Give the extent of all Plasmodium falciparum-infected red blood cells.
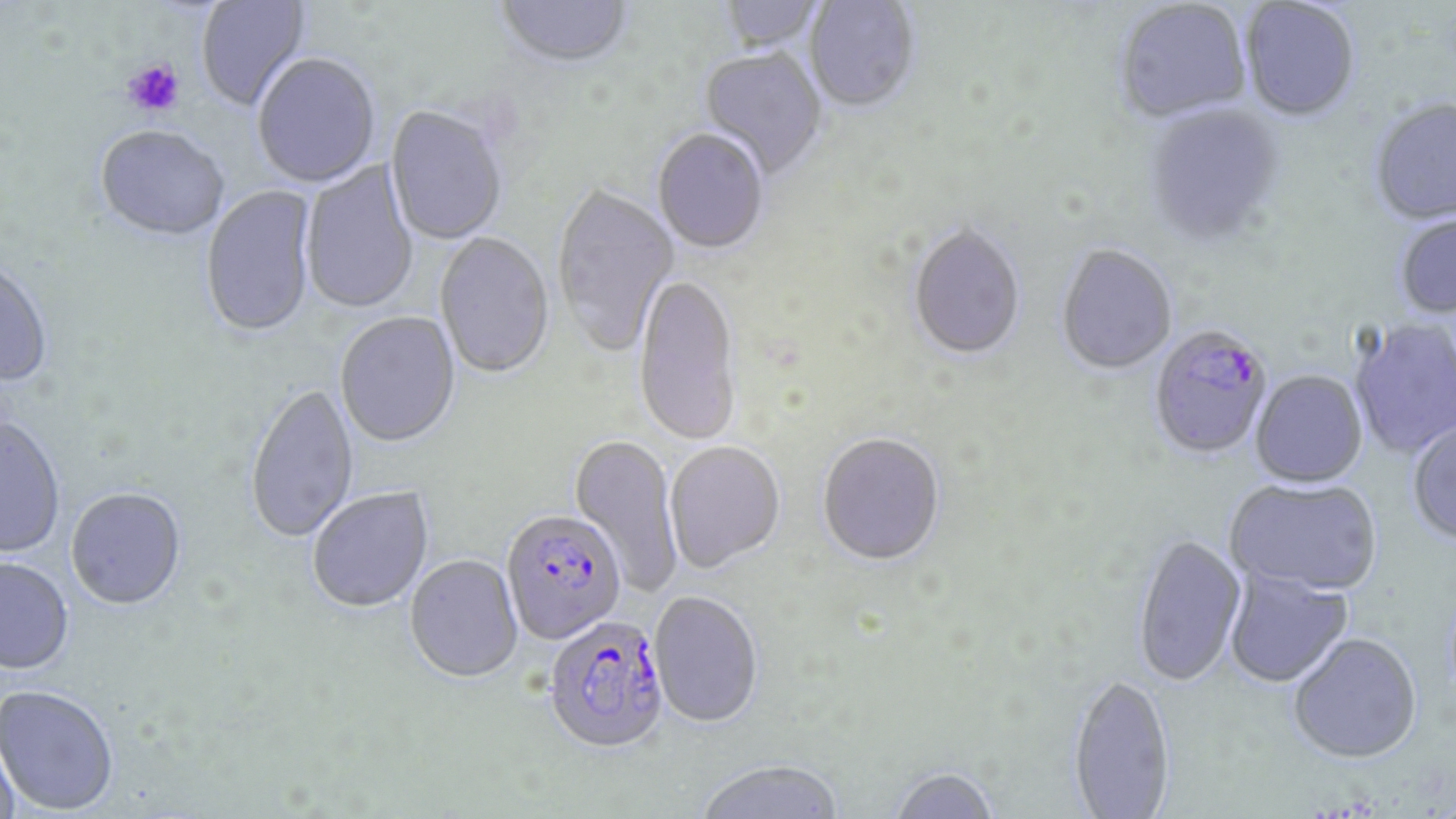
Approximate bounding boxes as named x1/y1/x2/y2 corners in pixels.
Plasmodium falciparum-infected red blood cells: (x1=1148, y1=328, x2=1274, y2=461), (x1=502, y1=513, x2=626, y2=647), (x1=543, y1=618, x2=670, y2=757).

Platelet locations: (x1=121, y1=58, x2=186, y2=118). Uninfected red blood cell locations: (x1=195, y1=1, x2=313, y2=114), (x1=495, y1=1, x2=635, y2=72), (x1=717, y1=1, x2=824, y2=55), (x1=804, y1=1, x2=920, y2=115), (x1=1115, y1=1, x2=1252, y2=125), (x1=1240, y1=1, x2=1360, y2=124), (x1=698, y1=49, x2=828, y2=181), (x1=252, y1=56, x2=381, y2=189), (x1=1370, y1=100, x2=1456, y2=228), (x1=1143, y1=105, x2=1284, y2=249), (x1=385, y1=107, x2=508, y2=246), (x1=94, y1=128, x2=229, y2=244), (x1=652, y1=130, x2=769, y2=255), (x1=300, y1=160, x2=419, y2=316), (x1=201, y1=185, x2=317, y2=341), (x1=551, y1=185, x2=679, y2=358), (x1=1395, y1=214, x2=1456, y2=320), (x1=908, y1=225, x2=1026, y2=364), (x1=434, y1=233, x2=555, y2=381), (x1=1056, y1=246, x2=1177, y2=377), (x1=0, y1=260, x2=54, y2=389), (x1=633, y1=276, x2=742, y2=448), (x1=335, y1=313, x2=461, y2=450), (x1=1348, y1=318, x2=1456, y2=461), (x1=1250, y1=371, x2=1368, y2=490), (x1=245, y1=384, x2=359, y2=545), (x1=0, y1=419, x2=66, y2=558), (x1=1407, y1=419, x2=1456, y2=547), (x1=569, y1=434, x2=682, y2=595), (x1=817, y1=434, x2=945, y2=569), (x1=664, y1=443, x2=786, y2=575), (x1=1225, y1=479, x2=1382, y2=598), (x1=307, y1=488, x2=434, y2=615), (x1=66, y1=489, x2=187, y2=613), (x1=1132, y1=535, x2=1247, y2=690), (x1=405, y1=556, x2=523, y2=685), (x1=0, y1=560, x2=74, y2=677), (x1=1223, y1=568, x2=1354, y2=689), (x1=648, y1=593, x2=763, y2=730), (x1=1288, y1=634, x2=1422, y2=764), (x1=1067, y1=676, x2=1176, y2=819), (x1=0, y1=687, x2=119, y2=816), (x1=0, y1=736, x2=19, y2=819), (x1=694, y1=761, x2=845, y2=819), (x1=888, y1=768, x2=1000, y2=818). Slide-level diagnosis: Plasmodium falciparum. Thin blood smear. Single field of view. May-Grünwald-Giemsa-stained preparation. Optical microscopy. Image is 1456×819 pixels. Captured at 1000x magnification.